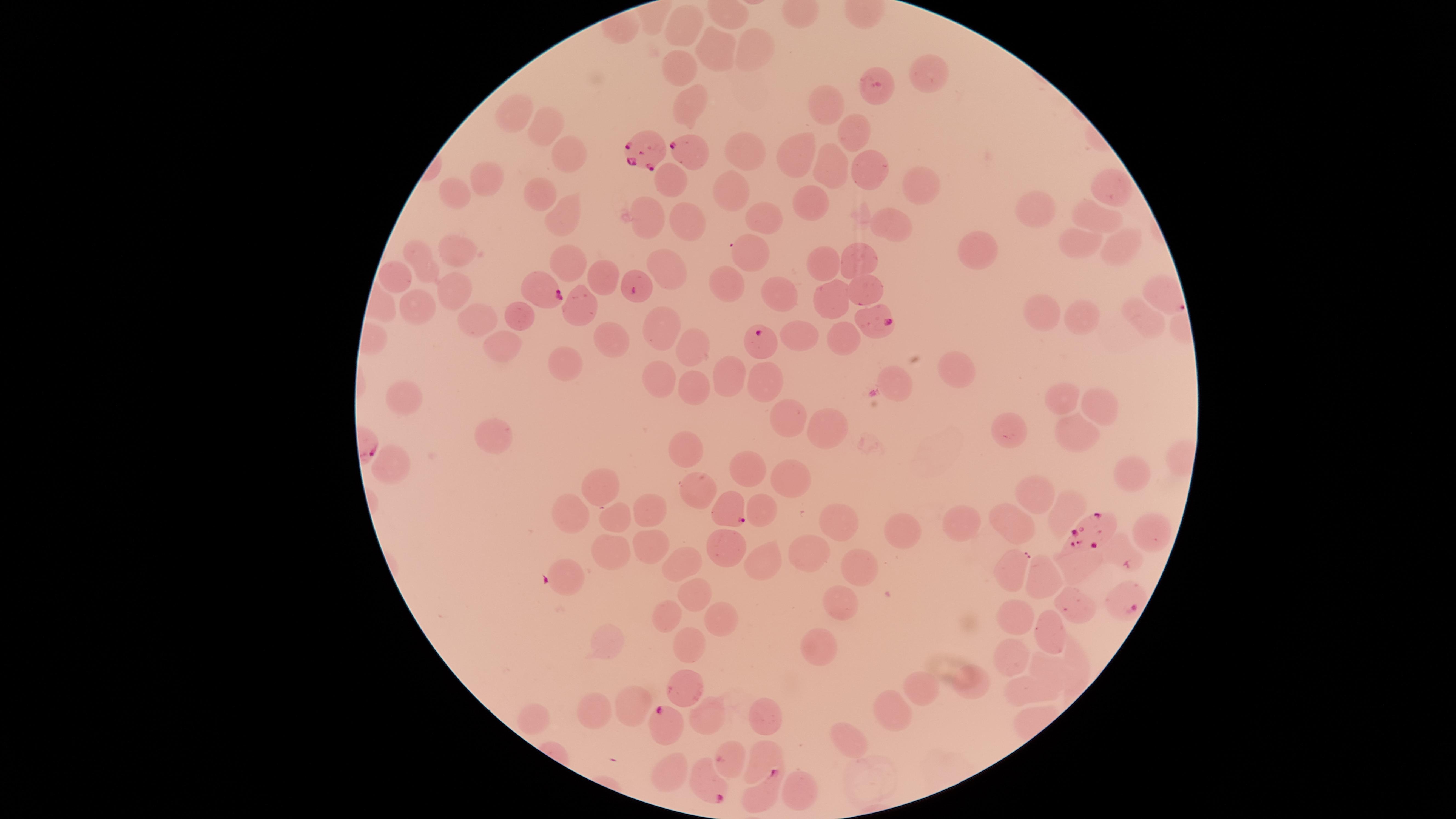
image size = 1456×819 pixels
uninfected red blood cells = approximate marker points, in pixels from the top-left corner: (x=690, y=21), (x=756, y=46), (x=713, y=54), (x=687, y=65), (x=928, y=72), (x=693, y=103), (x=826, y=110), (x=509, y=114), (x=545, y=126), (x=854, y=135), (x=747, y=151), (x=569, y=154), (x=799, y=155), (x=835, y=162), (x=871, y=168), (x=484, y=179), (x=672, y=179), (x=914, y=186), (x=734, y=188), (x=1109, y=190), (x=455, y=191), (x=544, y=191), (x=812, y=204), (x=1039, y=206), (x=562, y=208), (x=688, y=209), (x=1092, y=215), (x=762, y=217), (x=644, y=218), (x=891, y=231), (x=1076, y=242), (x=1115, y=243), (x=977, y=249), (x=463, y=254), (x=751, y=254), (x=865, y=256), (x=424, y=260), (x=567, y=263), (x=667, y=263), (x=823, y=264), (x=601, y=273), (x=392, y=275), (x=863, y=284), (x=726, y=288), (x=1156, y=291), (x=455, y=293), (x=781, y=296), (x=833, y=304), (x=420, y=306), (x=579, y=308), (x=474, y=311), (x=521, y=313), (x=1048, y=315), (x=1088, y=319), (x=1143, y=320), (x=662, y=326), (x=802, y=332), (x=612, y=333), (x=845, y=335), (x=694, y=344), (x=501, y=347), (x=563, y=360), (x=955, y=369), (x=653, y=375), (x=726, y=375), (x=891, y=377), (x=760, y=383), (x=693, y=386), (x=401, y=393), (x=1064, y=403), (x=1095, y=408), (x=791, y=415), (x=1010, y=426), (x=820, y=428), (x=1079, y=428), (x=491, y=434), (x=684, y=452), (x=747, y=462), (x=389, y=465), (x=1132, y=478), (x=693, y=482), (x=792, y=482), (x=605, y=484), (x=1039, y=491), (x=1071, y=507), (x=763, y=508), (x=654, y=509), (x=573, y=514), (x=615, y=516), (x=965, y=518), (x=837, y=520), (x=1152, y=528), (x=1012, y=529), (x=896, y=535), (x=724, y=540), (x=646, y=548), (x=1116, y=549), (x=811, y=552), (x=607, y=554), (x=762, y=559), (x=680, y=562), (x=858, y=565), (x=1078, y=566), (x=566, y=568), (x=1010, y=569), (x=1043, y=577), (x=695, y=585), (x=838, y=601), (x=1076, y=604), (x=715, y=611), (x=1013, y=611), (x=666, y=612), (x=1054, y=625), (x=690, y=636), (x=818, y=639), (x=601, y=643), (x=1016, y=656), (x=1051, y=664), (x=1080, y=664), (x=972, y=679), (x=920, y=683), (x=689, y=686), (x=1029, y=688), (x=625, y=699), (x=891, y=706), (x=597, y=711), (x=710, y=713), (x=763, y=713), (x=541, y=714), (x=847, y=739), (x=762, y=748), (x=728, y=761), (x=669, y=777), (x=808, y=790)
field of view = single
stain = Giemsa
visible region = circular
species = Plasmodium falciparum
preparation = thin smear of blood
capture = smartphone photograph through the microscope eyepiece
parasitized red blood cells = approximate marker points, in pixels from the top-left corner: (x=649, y=153), (x=692, y=154), (x=634, y=286), (x=547, y=294), (x=876, y=319), (x=763, y=339), (x=729, y=508), (x=1088, y=529), (x=1123, y=598), (x=663, y=720), (x=705, y=784), (x=762, y=797)
presence = malaria parasites detected